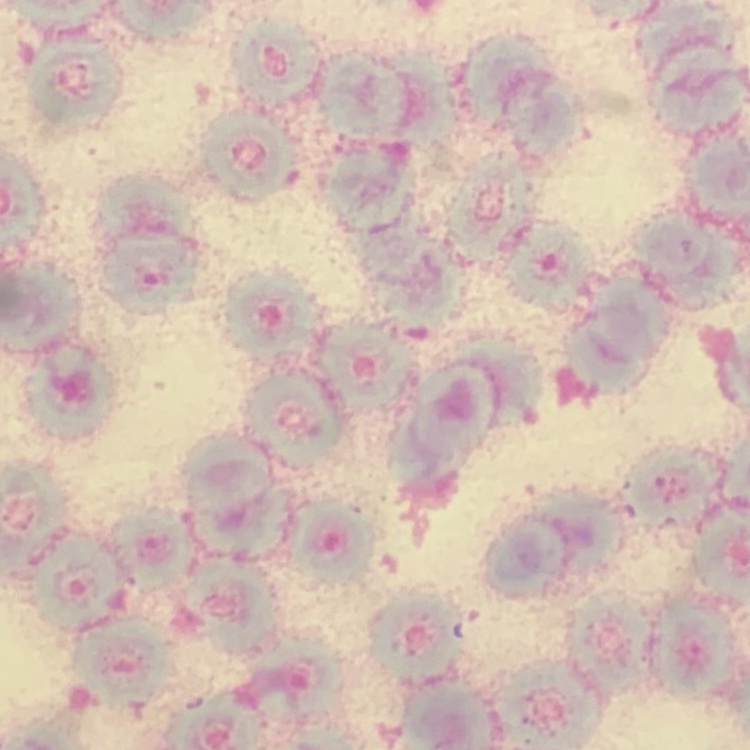

The erythrocytes show rouleaux formation. Thin blood smear. Field's or Giemsa stain. Square crop of a larger photomicrograph.